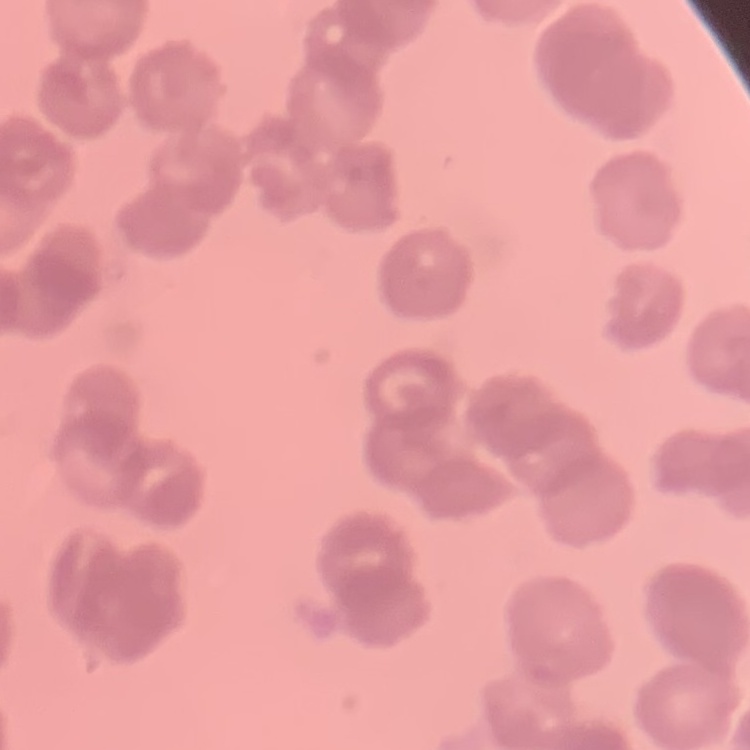
erythrocyte morphology = rouleaux formation
image type = one tile cut from a larger photomicrograph
preparation = thin peripheral smear
stain = Field's or Giemsa